Identify the blood parasite species.
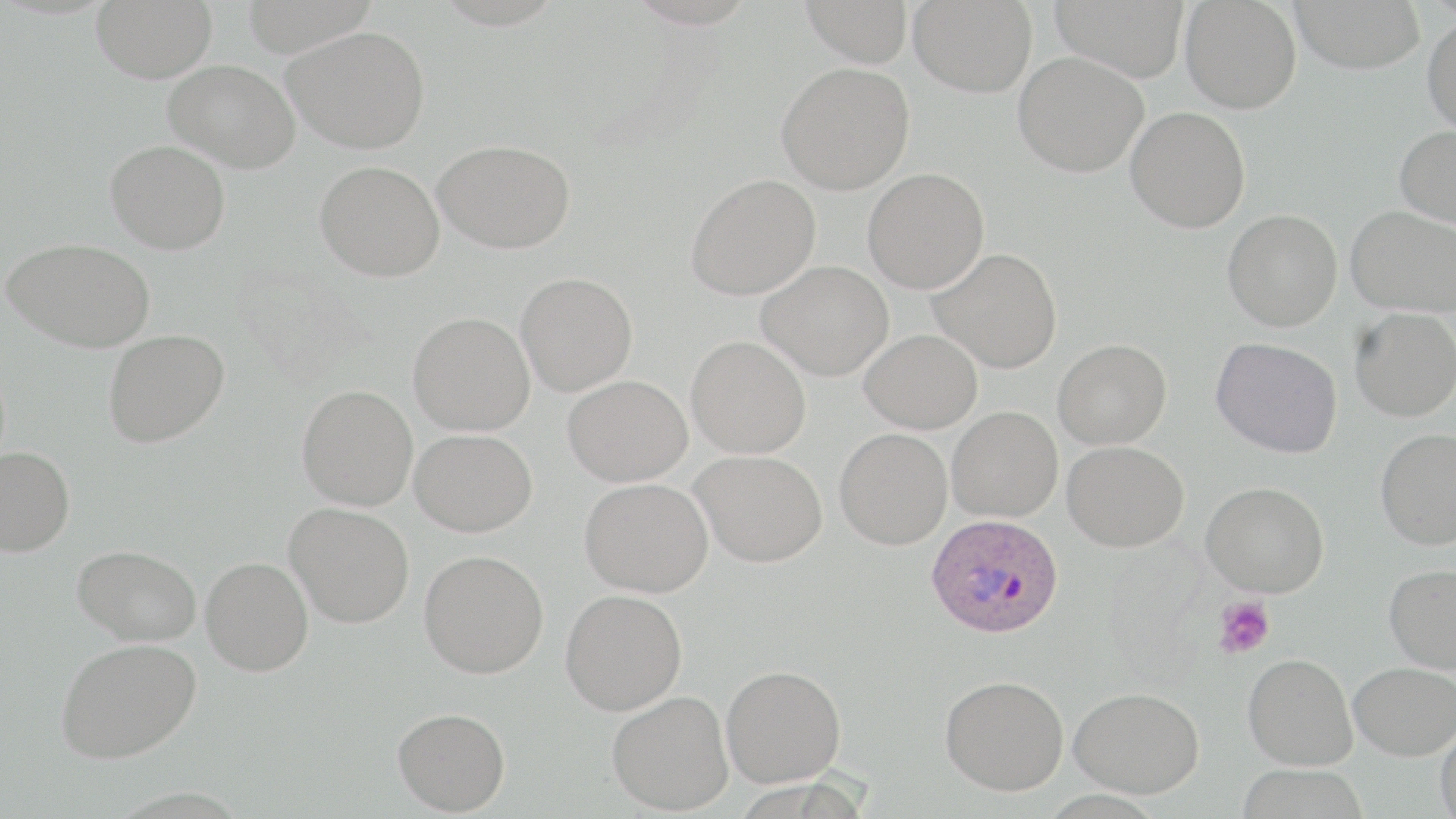
Plasmodium ovale.

Summary:
  - Coordinate format: approximate bounding boxes as [x1, y1, x2, y2] in pixels
  - Plasmodium ovale-infected red blood cell locations: [926, 514, 1063, 639]
  - Uninfected red blood cell locations: [91, 0, 217, 83], [801, 0, 913, 66], [909, 0, 1038, 97], [1050, 0, 1191, 82], [1180, 0, 1302, 114], [1290, 0, 1425, 74], [1422, 15, 1456, 137], [283, 25, 430, 153], [1013, 51, 1148, 177], [164, 59, 301, 173], [776, 62, 915, 194], [1125, 106, 1251, 233], [1394, 125, 1456, 229], [433, 139, 575, 254], [106, 140, 231, 254], [314, 160, 444, 281], [863, 168, 989, 294], [686, 174, 821, 300], [1346, 205, 1456, 317], [1223, 208, 1342, 331], [3, 238, 155, 353], [929, 248, 1062, 373], [757, 260, 894, 381], [515, 272, 637, 396], [1350, 307, 1456, 422], [407, 312, 535, 436], [102, 328, 230, 448], [860, 329, 982, 433], [686, 335, 811, 458], [1210, 337, 1343, 459], [1053, 338, 1171, 449], [563, 375, 692, 486], [296, 384, 418, 511], [947, 406, 1062, 522], [834, 428, 952, 549], [1375, 428, 1456, 550], [410, 429, 537, 537], [1062, 440, 1188, 552], [0, 445, 74, 556], [690, 449, 827, 567], [579, 478, 713, 597], [1201, 481, 1329, 597], [284, 501, 414, 627], [73, 544, 201, 646], [419, 550, 548, 678], [200, 557, 313, 676], [1384, 563, 1456, 673], [560, 589, 687, 715], [55, 637, 202, 763], [1243, 653, 1357, 770], [1348, 662, 1456, 761], [721, 664, 846, 786], [939, 674, 1069, 795], [1068, 687, 1204, 798], [607, 690, 733, 815], [392, 707, 510, 815], [1435, 722, 1456, 818], [1235, 763, 1370, 819]
  - Platelet locations: [1214, 596, 1275, 658]
  - Preparation: thin blood film
  - Field of view: single
  - Magnification: 1000x
  - Image size: 1456×819 pixels
  - Modality: light microscopy
  - Stain: May-Grünwald-Giemsa